Describe the morphology of the erythrocytes.
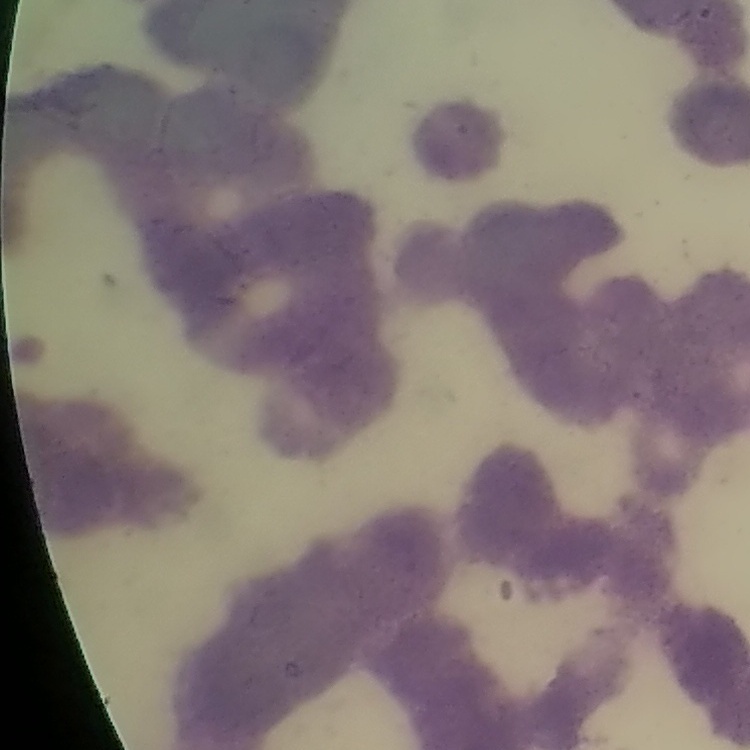
Rouleaux formation.

{
  "stain": "Field's or Giemsa",
  "image_type": "one tile cut from a larger photomicrograph",
  "preparation": "thin peripheral smear"
}